Report the malaria status of this cell.
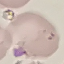
Parasitized.

{
  "stain": "Giemsa",
  "preparation": "thin blood smear",
  "capture": "smartphone through the microscope eyepiece",
  "image_type": "cell patch, automatically extracted from a larger field of view and resized to 64 × 64 pixels"
}